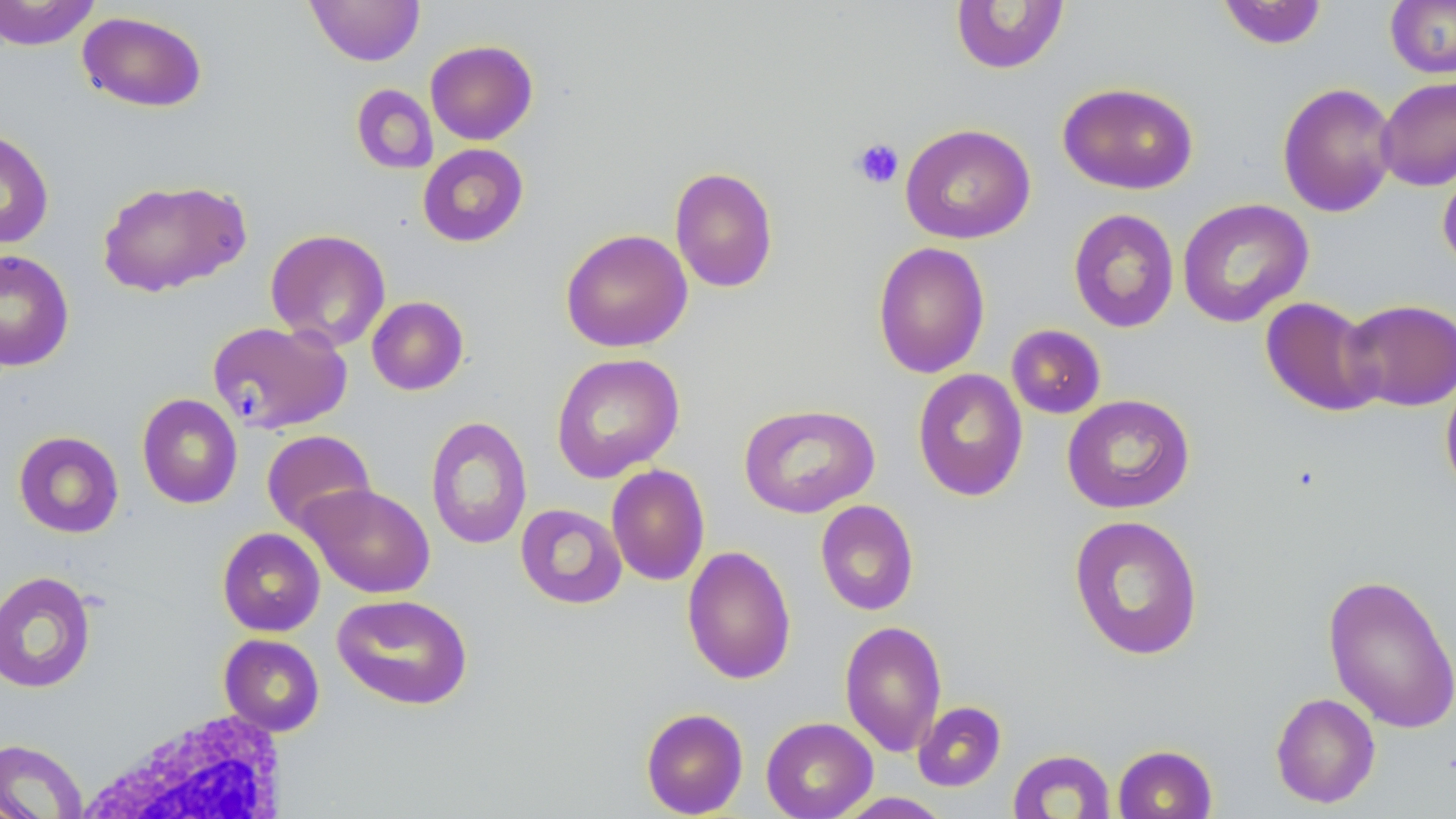
Approximate bounding boxes as named x1/y1/x2/y2 corners in pixels. White blood cell locations (subset): (x1=76, y1=708, x2=294, y2=818). Uninfected red blood cell locations (subset): (x1=0, y1=0, x2=101, y2=50), (x1=305, y1=0, x2=425, y2=66), (x1=1385, y1=0, x2=1456, y2=78), (x1=950, y1=1, x2=1069, y2=74), (x1=1216, y1=1, x2=1328, y2=50), (x1=77, y1=10, x2=208, y2=112), (x1=425, y1=40, x2=538, y2=145), (x1=1376, y1=76, x2=1456, y2=191), (x1=1057, y1=82, x2=1199, y2=194), (x1=1277, y1=82, x2=1399, y2=218), (x1=351, y1=84, x2=438, y2=175), (x1=900, y1=123, x2=1036, y2=244), (x1=0, y1=128, x2=54, y2=249), (x1=417, y1=144, x2=528, y2=247), (x1=1437, y1=153, x2=1456, y2=274), (x1=669, y1=166, x2=779, y2=293), (x1=96, y1=178, x2=250, y2=297), (x1=1177, y1=198, x2=1314, y2=328), (x1=1067, y1=208, x2=1180, y2=334), (x1=265, y1=229, x2=391, y2=351), (x1=560, y1=229, x2=692, y2=352), (x1=872, y1=241, x2=991, y2=379), (x1=0, y1=249, x2=75, y2=372), (x1=366, y1=296, x2=469, y2=395), (x1=1260, y1=297, x2=1383, y2=417), (x1=1342, y1=298, x2=1456, y2=412), (x1=208, y1=320, x2=351, y2=434), (x1=1005, y1=324, x2=1106, y2=419), (x1=550, y1=352, x2=685, y2=483), (x1=912, y1=368, x2=1029, y2=501), (x1=1440, y1=371, x2=1456, y2=498), (x1=136, y1=393, x2=243, y2=508), (x1=1062, y1=394, x2=1195, y2=514), (x1=738, y1=403, x2=880, y2=519), (x1=425, y1=415, x2=532, y2=550), (x1=261, y1=429, x2=376, y2=534), (x1=13, y1=431, x2=124, y2=538), (x1=606, y1=464, x2=710, y2=586), (x1=299, y1=483, x2=436, y2=598), (x1=814, y1=499, x2=919, y2=616), (x1=515, y1=503, x2=627, y2=609), (x1=1068, y1=514, x2=1204, y2=660), (x1=217, y1=527, x2=325, y2=636), (x1=682, y1=545, x2=796, y2=685), (x1=0, y1=570, x2=97, y2=693), (x1=1322, y1=573, x2=1456, y2=733), (x1=332, y1=593, x2=473, y2=710), (x1=839, y1=619, x2=947, y2=757), (x1=1270, y1=692, x2=1381, y2=808), (x1=913, y1=701, x2=1007, y2=792), (x1=641, y1=707, x2=748, y2=817), (x1=761, y1=716, x2=878, y2=819), (x1=0, y1=738, x2=88, y2=819), (x1=1112, y1=744, x2=1217, y2=819), (x1=1008, y1=749, x2=1116, y2=819), (x1=833, y1=792, x2=952, y2=819). Platelet locations: (x1=851, y1=137, x2=904, y2=189). Slide-level diagnosis: negative for blood parasites. May-Grünwald-Giemsa stain. Single field of view. Thin blood film. Image is 1456×819 pixels. Optical microscopy. 1000x magnification.